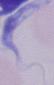

A trypanosome is shown. Micrograph. 1000x magnification.